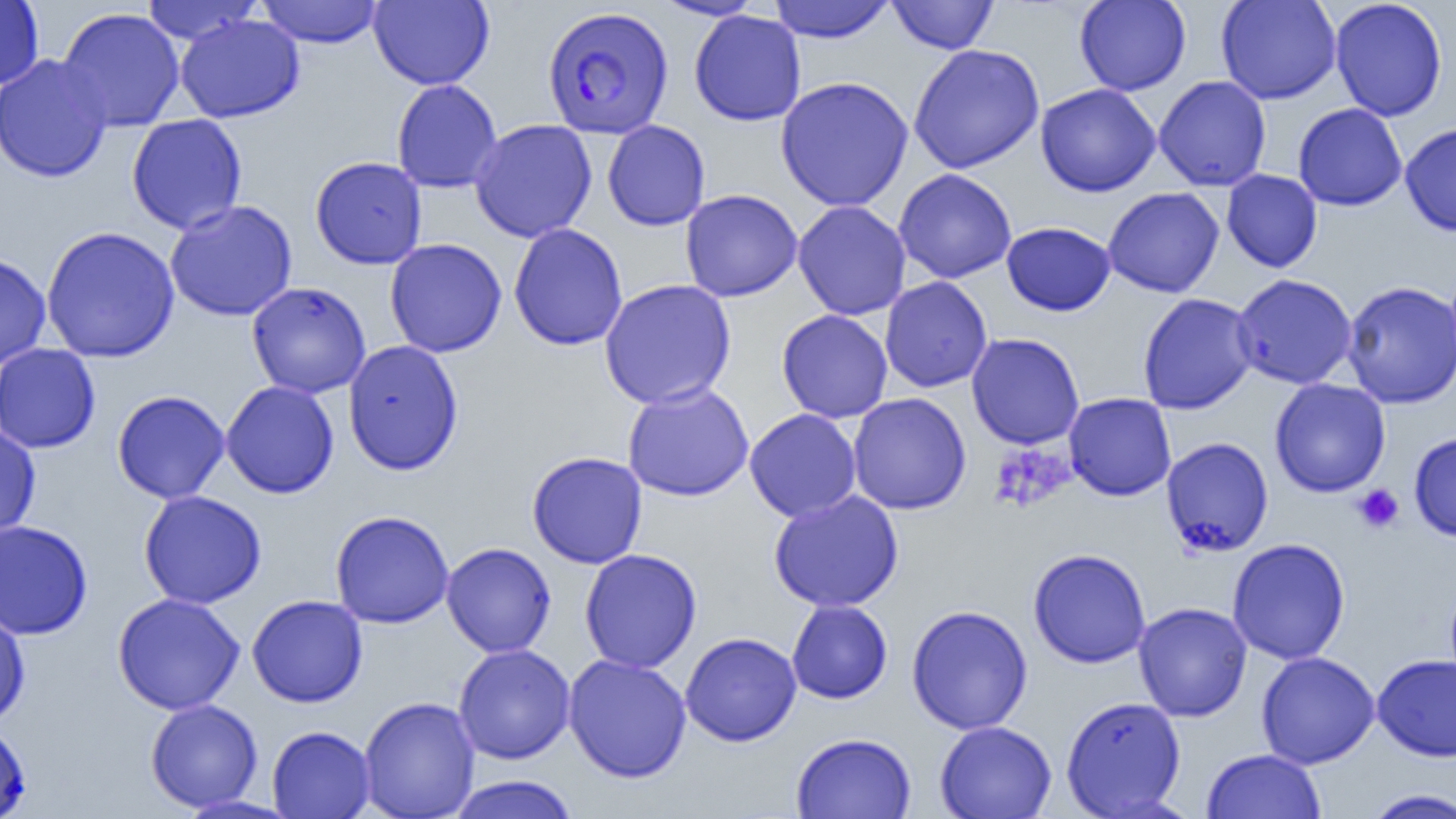

Summary:
  - Coordinate format: approximate bounding boxes as named x1/y1/x2/y2 corners in pixels
  - Platelet locations: (x1=990, y1=442, x2=1075, y2=513), (x1=1353, y1=484, x2=1404, y2=534)
  - Uninfected red blood cell locations: (x1=0, y1=0, x2=44, y2=90), (x1=255, y1=0, x2=385, y2=48), (x1=368, y1=0, x2=495, y2=90), (x1=652, y1=0, x2=766, y2=20), (x1=767, y1=0, x2=897, y2=43), (x1=887, y1=0, x2=999, y2=54), (x1=1074, y1=0, x2=1191, y2=96), (x1=1215, y1=0, x2=1342, y2=104), (x1=1330, y1=0, x2=1447, y2=122), (x1=141, y1=1, x2=265, y2=46), (x1=57, y1=7, x2=185, y2=132), (x1=689, y1=10, x2=806, y2=126), (x1=176, y1=15, x2=304, y2=123), (x1=907, y1=44, x2=1045, y2=174), (x1=0, y1=54, x2=113, y2=183), (x1=775, y1=76, x2=914, y2=212), (x1=1154, y1=76, x2=1272, y2=191), (x1=391, y1=79, x2=503, y2=193), (x1=1035, y1=83, x2=1161, y2=197), (x1=1292, y1=103, x2=1407, y2=211), (x1=126, y1=114, x2=247, y2=234), (x1=469, y1=119, x2=598, y2=243), (x1=602, y1=119, x2=710, y2=231), (x1=1400, y1=123, x2=1456, y2=236), (x1=310, y1=156, x2=427, y2=269), (x1=893, y1=168, x2=1017, y2=284), (x1=1221, y1=169, x2=1322, y2=273), (x1=1103, y1=186, x2=1225, y2=298), (x1=680, y1=189, x2=803, y2=302), (x1=164, y1=200, x2=297, y2=321), (x1=793, y1=201, x2=912, y2=321), (x1=1001, y1=221, x2=1116, y2=316), (x1=508, y1=223, x2=628, y2=351), (x1=40, y1=226, x2=180, y2=363), (x1=384, y1=238, x2=507, y2=357), (x1=0, y1=251, x2=52, y2=369), (x1=1231, y1=273, x2=1357, y2=390), (x1=879, y1=277, x2=992, y2=393), (x1=598, y1=279, x2=737, y2=410), (x1=1342, y1=280, x2=1456, y2=409), (x1=246, y1=281, x2=371, y2=398), (x1=1137, y1=293, x2=1258, y2=415), (x1=776, y1=309, x2=893, y2=423), (x1=966, y1=333, x2=1084, y2=449), (x1=343, y1=340, x2=464, y2=476), (x1=0, y1=343, x2=101, y2=453), (x1=1269, y1=378, x2=1391, y2=498), (x1=221, y1=380, x2=340, y2=499), (x1=622, y1=381, x2=754, y2=501), (x1=112, y1=390, x2=230, y2=504), (x1=1064, y1=392, x2=1176, y2=501), (x1=847, y1=393, x2=971, y2=515), (x1=744, y1=408, x2=862, y2=522), (x1=0, y1=421, x2=41, y2=541), (x1=1408, y1=431, x2=1456, y2=542), (x1=1161, y1=437, x2=1274, y2=557), (x1=527, y1=451, x2=648, y2=569), (x1=138, y1=490, x2=267, y2=609), (x1=767, y1=490, x2=904, y2=613), (x1=330, y1=510, x2=454, y2=628), (x1=0, y1=519, x2=93, y2=639), (x1=1227, y1=537, x2=1351, y2=665), (x1=441, y1=542, x2=557, y2=657), (x1=579, y1=548, x2=702, y2=673), (x1=1028, y1=548, x2=1152, y2=669), (x1=112, y1=593, x2=245, y2=715), (x1=246, y1=594, x2=369, y2=708), (x1=786, y1=599, x2=893, y2=704), (x1=1133, y1=602, x2=1252, y2=721), (x1=906, y1=605, x2=1033, y2=734), (x1=0, y1=608, x2=30, y2=727), (x1=680, y1=631, x2=802, y2=747), (x1=453, y1=644, x2=576, y2=764), (x1=1256, y1=651, x2=1380, y2=769), (x1=1372, y1=653, x2=1456, y2=762), (x1=563, y1=654, x2=692, y2=783), (x1=1060, y1=695, x2=1187, y2=818), (x1=358, y1=696, x2=480, y2=819), (x1=144, y1=698, x2=263, y2=812), (x1=0, y1=720, x2=31, y2=818), (x1=934, y1=720, x2=1057, y2=819), (x1=266, y1=725, x2=375, y2=818), (x1=791, y1=732, x2=917, y2=819), (x1=1202, y1=749, x2=1325, y2=819), (x1=446, y1=775, x2=580, y2=819), (x1=1361, y1=788, x2=1456, y2=818)
  - Plasmodium falciparum-infected red blood cell locations: (x1=542, y1=6, x2=673, y2=139)
  - Slide-level diagnosis: Plasmodium falciparum
  - Image size: 1456×819 pixels
  - Field of view: single
  - Preparation: thin blood film
  - Modality: light microscopy
  - Magnification: 1000x